Assess this cell for malaria.
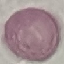
Uninfected.

Summary:
  - Capture: smartphone camera at the microscope eyepiece
  - Preparation: thin smear
  - Stain: Giemsa
  - Image type: automatically extracted cell patch, resized to 64 × 64 pixels